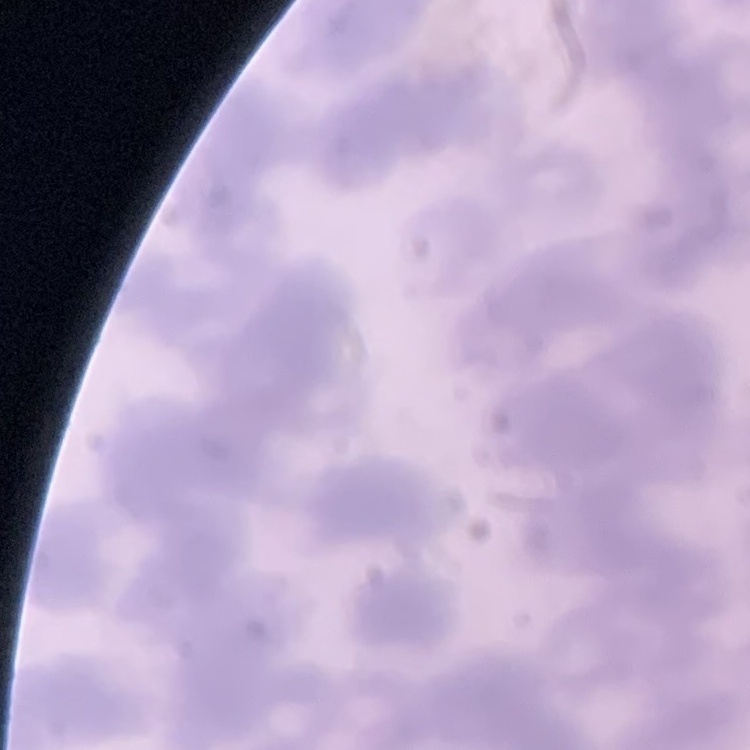

The red blood cells exhibit rouleaux formation. Field's or Giemsa stain. Thin blood film. One tile cut from a larger photomicrograph.